Identify the blood parasite species.
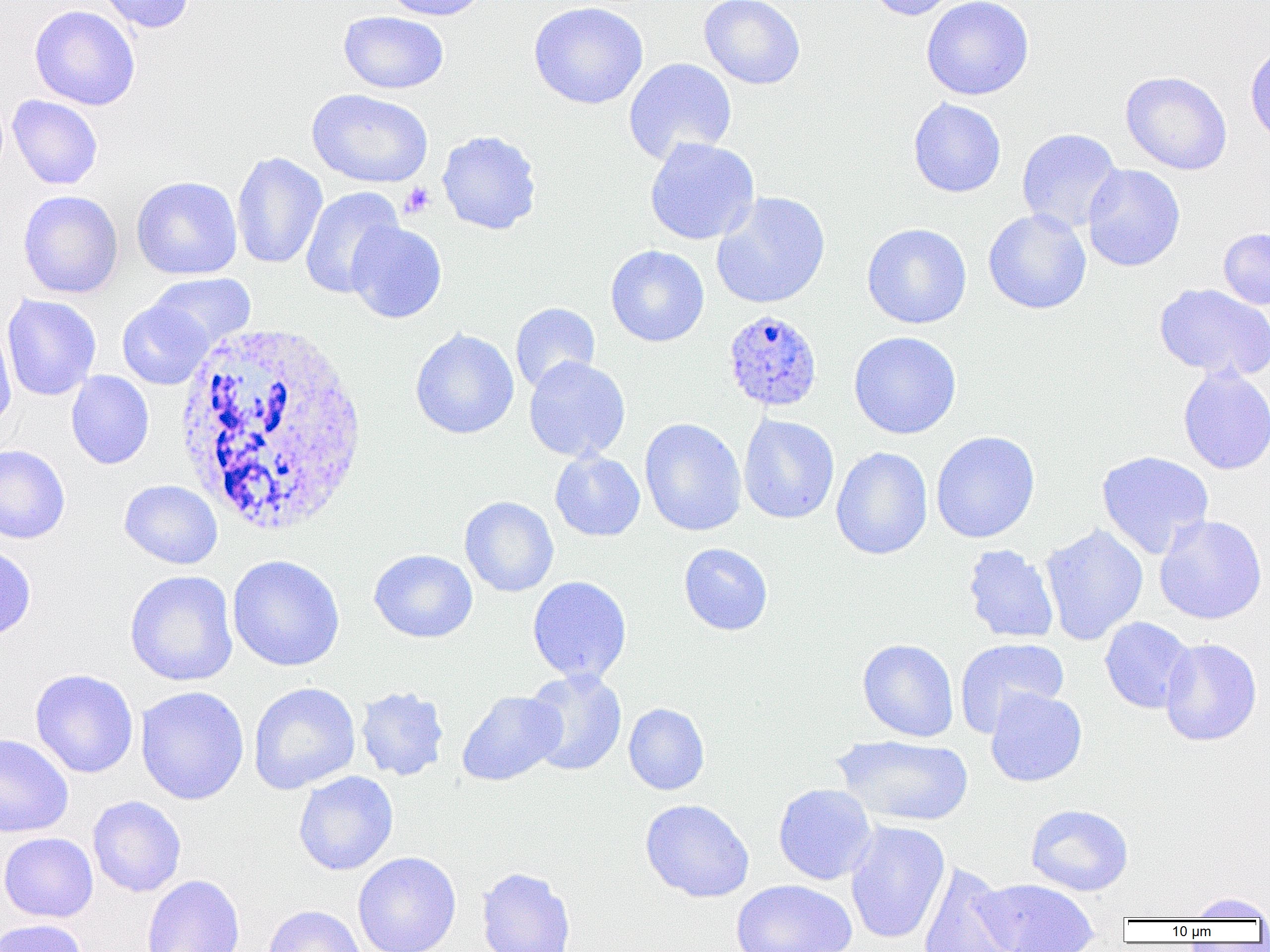
Plasmodium ovale.

Approximate bounding boxes as named x1/y1/x2/y2 corners in pixels. Platelet locations: (x1=400, y1=182, x2=435, y2=218). Plasmodium ovale-infected red blood cell locations: (x1=722, y1=309, x2=823, y2=412). White blood cell locations: (x1=172, y1=321, x2=373, y2=537). Uninfected red blood cell locations: (x1=95, y1=0, x2=195, y2=34), (x1=380, y1=0, x2=490, y2=21), (x1=699, y1=0, x2=806, y2=90), (x1=863, y1=0, x2=962, y2=21), (x1=921, y1=0, x2=1034, y2=101), (x1=529, y1=1, x2=649, y2=109), (x1=917, y1=1, x2=1019, y2=200), (x1=29, y1=5, x2=141, y2=111), (x1=338, y1=11, x2=449, y2=94), (x1=1245, y1=40, x2=1270, y2=146), (x1=624, y1=58, x2=737, y2=164), (x1=1120, y1=70, x2=1232, y2=175), (x1=307, y1=88, x2=433, y2=188), (x1=7, y1=95, x2=103, y2=190), (x1=907, y1=97, x2=1006, y2=198), (x1=1017, y1=128, x2=1122, y2=234), (x1=437, y1=130, x2=542, y2=235), (x1=644, y1=137, x2=760, y2=245), (x1=231, y1=152, x2=328, y2=270), (x1=1082, y1=164, x2=1185, y2=272), (x1=131, y1=176, x2=243, y2=280), (x1=299, y1=186, x2=404, y2=299), (x1=18, y1=190, x2=123, y2=299), (x1=711, y1=192, x2=831, y2=309), (x1=983, y1=208, x2=1092, y2=314), (x1=346, y1=221, x2=447, y2=323), (x1=862, y1=223, x2=972, y2=329), (x1=1218, y1=227, x2=1270, y2=309), (x1=606, y1=245, x2=709, y2=347), (x1=148, y1=273, x2=255, y2=351), (x1=1154, y1=283, x2=1270, y2=382), (x1=2, y1=294, x2=101, y2=401), (x1=117, y1=299, x2=213, y2=390), (x1=510, y1=302, x2=600, y2=394), (x1=0, y1=322, x2=17, y2=433), (x1=410, y1=328, x2=519, y2=439), (x1=849, y1=331, x2=961, y2=439), (x1=523, y1=356, x2=631, y2=462), (x1=1178, y1=365, x2=1270, y2=475), (x1=66, y1=371, x2=154, y2=469), (x1=738, y1=414, x2=839, y2=524), (x1=639, y1=418, x2=747, y2=537), (x1=930, y1=431, x2=1040, y2=543), (x1=0, y1=444, x2=70, y2=544), (x1=831, y1=447, x2=933, y2=560), (x1=550, y1=450, x2=646, y2=542), (x1=1096, y1=450, x2=1214, y2=559), (x1=119, y1=479, x2=223, y2=569), (x1=459, y1=496, x2=559, y2=597), (x1=1154, y1=514, x2=1267, y2=625), (x1=1040, y1=524, x2=1148, y2=646), (x1=678, y1=543, x2=773, y2=636), (x1=0, y1=544, x2=36, y2=641), (x1=962, y1=544, x2=1060, y2=643), (x1=369, y1=549, x2=478, y2=643), (x1=226, y1=555, x2=345, y2=672), (x1=125, y1=570, x2=239, y2=687), (x1=527, y1=576, x2=632, y2=684), (x1=1099, y1=617, x2=1196, y2=714), (x1=955, y1=637, x2=1069, y2=736), (x1=857, y1=638, x2=959, y2=742), (x1=1159, y1=638, x2=1263, y2=746), (x1=29, y1=668, x2=139, y2=779), (x1=522, y1=668, x2=627, y2=776), (x1=248, y1=682, x2=361, y2=795), (x1=135, y1=685, x2=249, y2=805), (x1=355, y1=685, x2=450, y2=781), (x1=985, y1=688, x2=1087, y2=787), (x1=456, y1=691, x2=565, y2=786), (x1=623, y1=703, x2=710, y2=795), (x1=0, y1=732, x2=74, y2=838), (x1=831, y1=735, x2=974, y2=828), (x1=293, y1=771, x2=399, y2=876), (x1=773, y1=783, x2=878, y2=885), (x1=87, y1=796, x2=186, y2=897), (x1=640, y1=799, x2=755, y2=903), (x1=1025, y1=804, x2=1133, y2=896), (x1=844, y1=820, x2=950, y2=944), (x1=0, y1=832, x2=99, y2=923), (x1=353, y1=852, x2=461, y2=952), (x1=917, y1=862, x2=1018, y2=952), (x1=476, y1=866, x2=577, y2=952), (x1=141, y1=875, x2=245, y2=952), (x1=973, y1=878, x2=1099, y2=952), (x1=731, y1=879, x2=857, y2=952), (x1=1184, y1=892, x2=1270, y2=921), (x1=263, y1=905, x2=366, y2=952), (x1=1, y1=918, x2=89, y2=952). 1000x magnification. One field of a larger specimen. Thin blood smear. Image is 1270×952 pixels. Light microscopy.